Identify the preparation type.
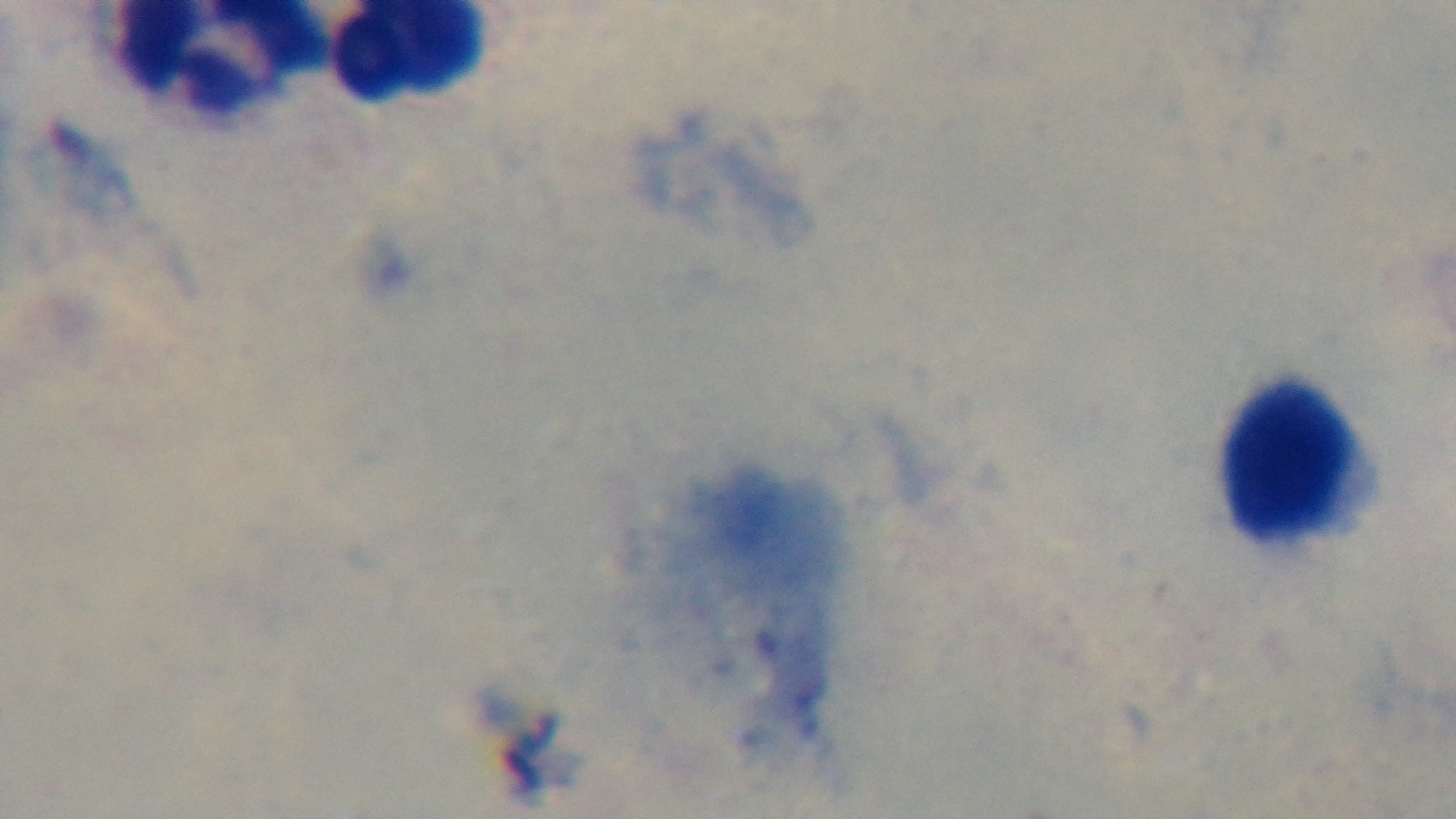
Thick.

Summary:
  - Capture: mounted 4K digital camera
  - Field of view: one from the slide
  - Objective: 100x oil immersion
  - Modality: light microscopy
  - Stain: Giemsa
  - Malaria status: uninfected